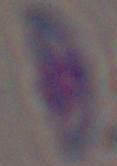

identification: Toxoplasma gondii
magnification: 1000x
modality: photomicrograph